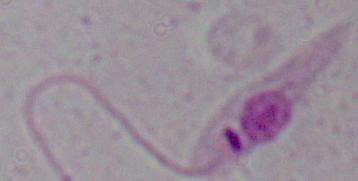

Summary:
  - Magnification: 1000x
  - Modality: micrograph
  - Identification: Leishmania